Assess this cell for malaria.
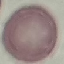
Uninfected.

Summary:
  - Capture: smartphone through the microscope eyepiece
  - Stain: Giemsa
  - Image type: automatically extracted cell patch, resized to 64 × 64 pixels
  - Preparation: thin blood film